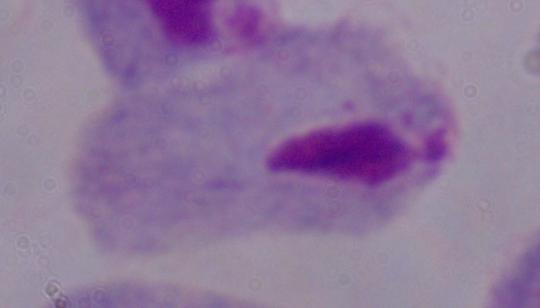

identification = trichomonad
modality = photomicrograph
magnification = 1000x